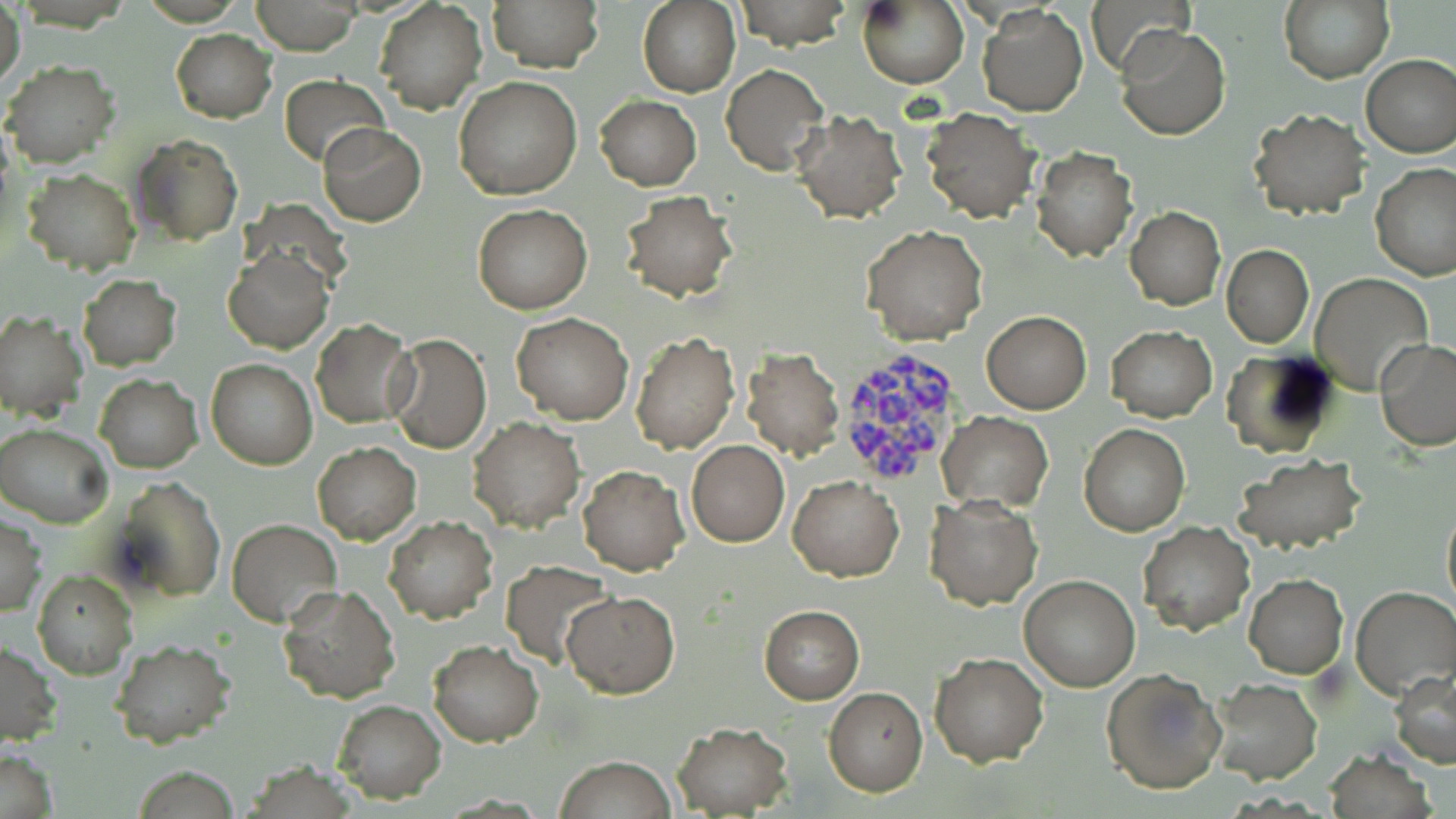

Approximate bounding boxes as (x1, y1, x2, y2) in pixels. Plasmodium vivax-infected red blood cell locations: (835, 347, 968, 490). Uninfected red blood cell locations: (248, 0, 364, 55), (487, 0, 603, 72), (734, 0, 850, 50), (858, 0, 968, 88), (1086, 0, 1194, 77), (1279, 0, 1394, 83), (0, 1, 25, 94), (374, 1, 487, 115), (638, 1, 740, 98), (977, 4, 1088, 116), (1115, 27, 1230, 141), (170, 30, 276, 123), (1360, 54, 1456, 158), (3, 60, 121, 170), (721, 64, 828, 176), (278, 73, 388, 168), (454, 76, 583, 201), (596, 94, 701, 190), (921, 108, 1038, 223), (790, 109, 906, 223), (1248, 109, 1368, 221), (317, 123, 426, 227), (131, 134, 242, 245), (1032, 147, 1137, 262), (1370, 162, 1456, 281), (22, 168, 139, 274), (621, 189, 740, 302), (472, 204, 593, 314), (1125, 207, 1225, 309), (861, 224, 987, 347), (1221, 246, 1314, 348), (224, 249, 333, 353), (77, 274, 181, 371), (1311, 274, 1433, 393), (0, 309, 89, 420), (512, 311, 634, 425), (981, 311, 1091, 414), (311, 319, 413, 426), (1105, 327, 1216, 421), (386, 332, 492, 454), (630, 332, 739, 455), (1374, 339, 1456, 451), (740, 347, 844, 461), (1221, 351, 1341, 460), (206, 359, 317, 471), (95, 374, 202, 473), (936, 410, 1053, 511), (467, 418, 585, 534), (1078, 423, 1190, 536), (1, 424, 115, 527), (685, 439, 789, 547), (313, 442, 421, 545), (1235, 454, 1366, 554), (577, 464, 689, 576), (788, 473, 904, 582), (111, 476, 225, 602), (923, 493, 1044, 610), (1442, 501, 1456, 612), (1, 514, 45, 616), (384, 515, 497, 624), (228, 519, 342, 626), (1138, 522, 1255, 634), (502, 561, 614, 667), (33, 571, 137, 678), (1019, 573, 1141, 692), (1244, 575, 1348, 679), (276, 583, 401, 702), (1351, 585, 1456, 698), (562, 590, 679, 698), (759, 605, 863, 704), (109, 639, 237, 750), (430, 639, 543, 747), (0, 641, 59, 746), (929, 651, 1050, 767), (1100, 666, 1225, 794), (1390, 668, 1456, 769), (1207, 678, 1322, 784), (823, 686, 928, 796), (332, 699, 446, 802), (673, 722, 792, 816), (0, 747, 57, 819), (1323, 751, 1434, 819), (555, 755, 676, 819), (130, 766, 244, 818). Slide-level diagnosis: Plasmodium vivax. 1000x magnification. Light microscopy. One field of a larger specimen. May-Grünwald-Giemsa-stained preparation. Thin blood film. Image is 1456×819 pixels.